Name the parasite shown.
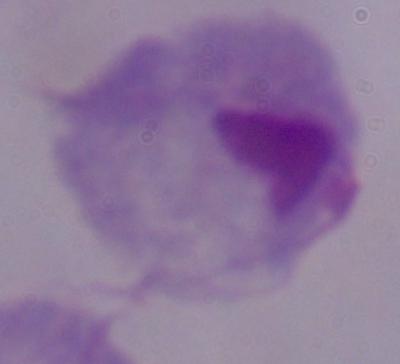

This is a trichomonad.

Summary:
  - Magnification: 1000x
  - Modality: photomicrograph